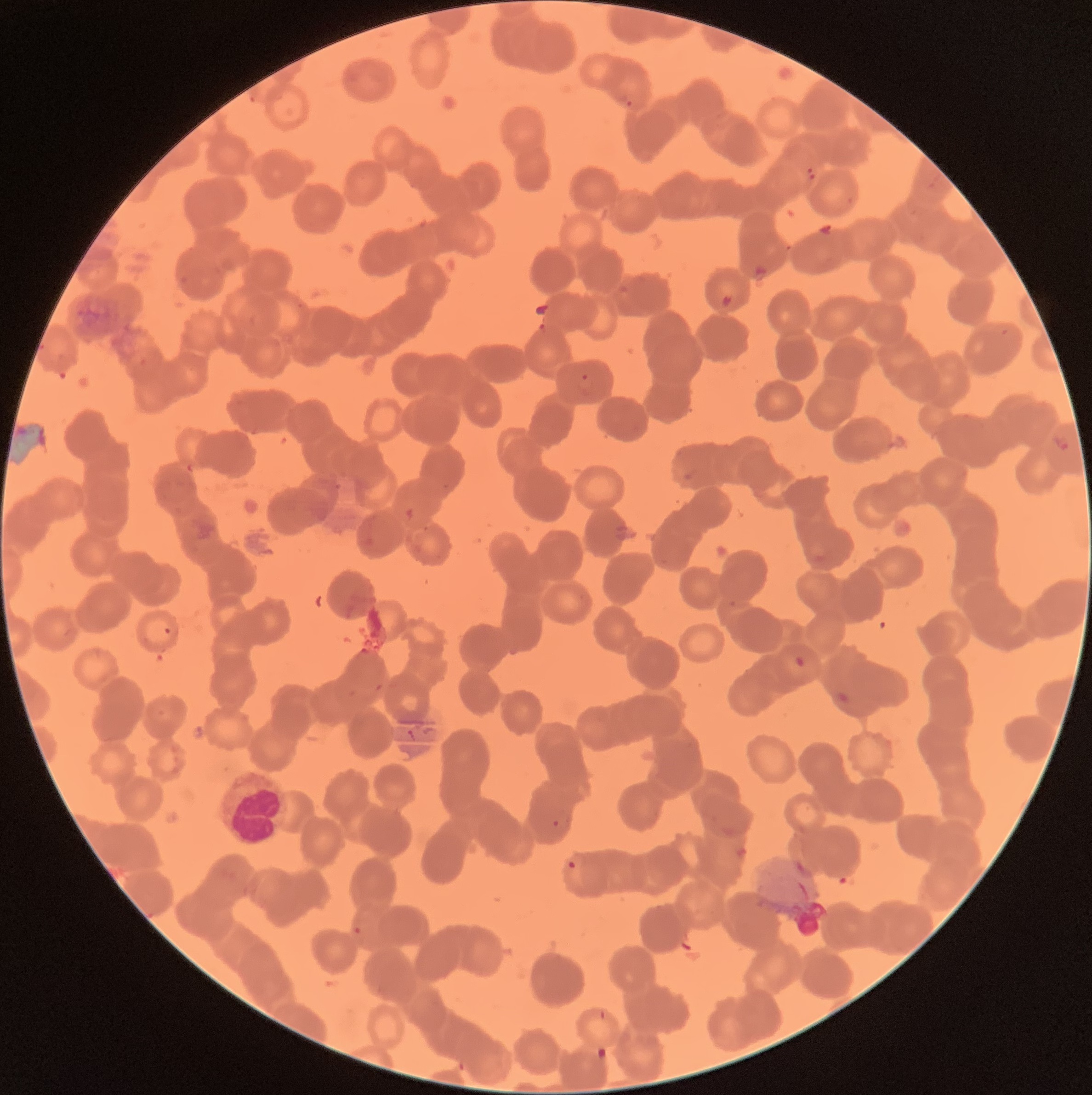
Summary:
  - Coordinate format: approximate bounding boxes as (x1, y1, x2, y2) in pixels
  - Plasmodium parasite locations: (625, 98, 634, 110), (805, 166, 817, 182), (576, 371, 595, 398), (1055, 434, 1072, 453), (163, 626, 172, 636), (794, 655, 805, 669), (550, 818, 561, 830), (567, 859, 577, 871), (352, 925, 363, 936), (597, 1008, 609, 1023)
  - White blood cell locations: (220, 772, 289, 842)
  - Preparation: thin blood smear
  - Red blood cell morphology: rouleaux formation
  - Modality: optical microscopy
  - Image size: 1092×1095 pixels